Identify the parasite.
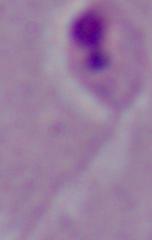

This is Leishmania.

Summary:
  - Magnification: 1000x
  - Modality: micrograph